Outline each blood parasite and name the species.
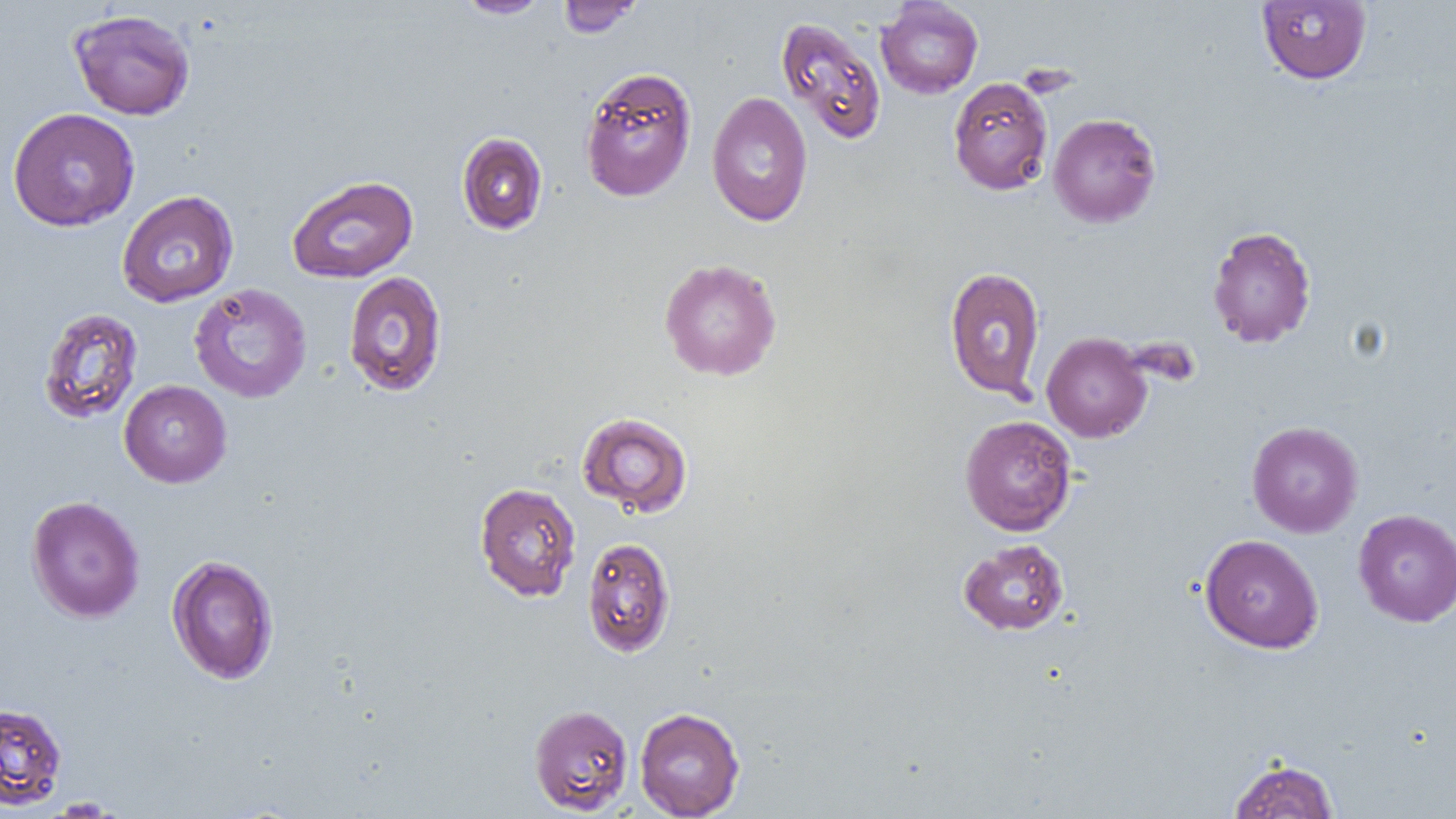
No blood parasites observed.

Summary:
  - Coordinate format: approximate bounding boxes as named x1/y1/x2/y2 corners in pixels
  - Uninfected red blood cell locations: (x1=455, y1=0, x2=552, y2=18), (x1=557, y1=0, x2=643, y2=38), (x1=875, y1=0, x2=984, y2=99), (x1=1256, y1=0, x2=1372, y2=85), (x1=68, y1=9, x2=196, y2=121), (x1=776, y1=17, x2=887, y2=145), (x1=579, y1=65, x2=698, y2=203), (x1=948, y1=76, x2=1054, y2=196), (x1=706, y1=92, x2=813, y2=227), (x1=8, y1=107, x2=140, y2=232), (x1=1047, y1=113, x2=1162, y2=228), (x1=457, y1=132, x2=547, y2=235), (x1=287, y1=174, x2=418, y2=283), (x1=116, y1=190, x2=239, y2=308), (x1=1206, y1=225, x2=1316, y2=349), (x1=658, y1=258, x2=783, y2=381), (x1=943, y1=266, x2=1046, y2=401), (x1=342, y1=270, x2=448, y2=397), (x1=189, y1=282, x2=312, y2=403), (x1=38, y1=307, x2=143, y2=424), (x1=1041, y1=331, x2=1152, y2=443), (x1=119, y1=380, x2=232, y2=488), (x1=576, y1=412, x2=693, y2=517), (x1=959, y1=414, x2=1077, y2=536), (x1=1247, y1=421, x2=1364, y2=538), (x1=474, y1=482, x2=581, y2=602), (x1=25, y1=495, x2=145, y2=623), (x1=1353, y1=509, x2=1456, y2=627), (x1=1199, y1=534, x2=1324, y2=653), (x1=582, y1=537, x2=676, y2=657), (x1=958, y1=539, x2=1069, y2=635), (x1=167, y1=554, x2=280, y2=685), (x1=0, y1=703, x2=67, y2=809), (x1=529, y1=704, x2=634, y2=815), (x1=634, y1=706, x2=745, y2=818), (x1=1228, y1=757, x2=1340, y2=818)
  - Slide-level diagnosis: no evidence of blood parasites
  - Image size: 1456×819 pixels
  - Field of view: one of a larger specimen
  - Modality: light microscopy
  - Preparation: thin blood film
  - Magnification: 1000x